Report the malaria status of this cell.
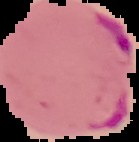
It is parasitized.

{
  "image_type": "segmented cell region on a black background",
  "preparation": "thin blood smear",
  "image_size": "139×142 pixels"
}